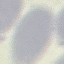 Result: no malaria parasites detected. Acquired by smartphone through the microscope eyepiece. Thin blood film. Automatically extracted cell patch, resized to 64 × 64 pixels. Giemsa stain.